State the blood parasite species.
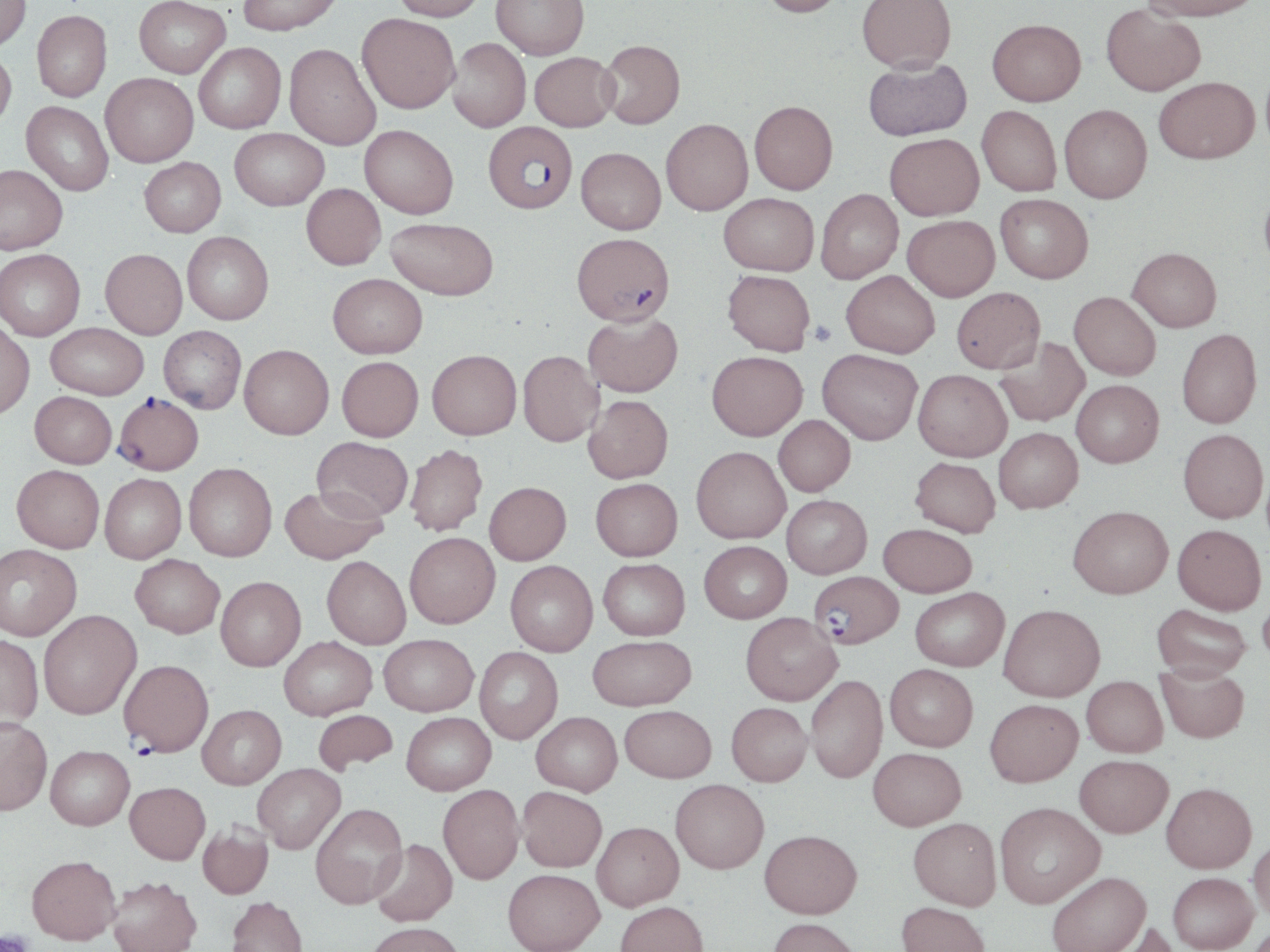

Plasmodium falciparum.

Summary:
  - Coordinate format: approximate bounding boxes as named x1/y1/x2/y2 corners in pixels
  - Platelet locations: (x1=809, y1=320, x2=837, y2=347), (x1=0, y1=931, x2=35, y2=952)
  - Uninfected red blood cell locations: (x1=0, y1=0, x2=31, y2=52), (x1=134, y1=0, x2=230, y2=77), (x1=238, y1=0, x2=343, y2=35), (x1=392, y1=0, x2=487, y2=21), (x1=491, y1=0, x2=589, y2=59), (x1=759, y1=0, x2=847, y2=17), (x1=857, y1=0, x2=956, y2=72), (x1=1142, y1=0, x2=1262, y2=21), (x1=1101, y1=4, x2=1206, y2=96), (x1=32, y1=10, x2=112, y2=101), (x1=357, y1=14, x2=460, y2=113), (x1=987, y1=18, x2=1086, y2=106), (x1=448, y1=38, x2=531, y2=132), (x1=599, y1=40, x2=685, y2=128), (x1=194, y1=42, x2=286, y2=133), (x1=285, y1=44, x2=381, y2=150), (x1=0, y1=49, x2=16, y2=130), (x1=529, y1=51, x2=619, y2=131), (x1=863, y1=57, x2=972, y2=141), (x1=101, y1=73, x2=198, y2=167), (x1=1154, y1=77, x2=1259, y2=163), (x1=750, y1=100, x2=838, y2=194), (x1=21, y1=101, x2=114, y2=196), (x1=1059, y1=104, x2=1152, y2=203), (x1=977, y1=105, x2=1062, y2=196), (x1=661, y1=118, x2=753, y2=215), (x1=360, y1=124, x2=458, y2=219), (x1=230, y1=128, x2=328, y2=210), (x1=885, y1=133, x2=984, y2=220), (x1=576, y1=147, x2=666, y2=234), (x1=140, y1=157, x2=225, y2=237), (x1=0, y1=164, x2=68, y2=255), (x1=1259, y1=182, x2=1270, y2=281), (x1=301, y1=183, x2=385, y2=269), (x1=816, y1=189, x2=903, y2=283), (x1=719, y1=192, x2=819, y2=275), (x1=995, y1=193, x2=1093, y2=282), (x1=902, y1=215, x2=1000, y2=301), (x1=385, y1=218, x2=498, y2=300), (x1=182, y1=231, x2=274, y2=324), (x1=1128, y1=247, x2=1222, y2=332), (x1=0, y1=249, x2=85, y2=340), (x1=100, y1=249, x2=188, y2=338), (x1=723, y1=270, x2=815, y2=355), (x1=842, y1=270, x2=940, y2=358), (x1=328, y1=273, x2=427, y2=358), (x1=951, y1=287, x2=1045, y2=373), (x1=1069, y1=291, x2=1161, y2=379), (x1=583, y1=312, x2=683, y2=397), (x1=0, y1=321, x2=35, y2=418), (x1=46, y1=322, x2=148, y2=399), (x1=158, y1=326, x2=246, y2=413), (x1=1176, y1=328, x2=1262, y2=428), (x1=994, y1=336, x2=1089, y2=426), (x1=239, y1=344, x2=333, y2=439), (x1=817, y1=348, x2=922, y2=444), (x1=427, y1=349, x2=521, y2=439), (x1=518, y1=350, x2=604, y2=446), (x1=707, y1=350, x2=807, y2=440), (x1=337, y1=356, x2=423, y2=441), (x1=913, y1=369, x2=1012, y2=461), (x1=1072, y1=380, x2=1163, y2=467), (x1=30, y1=391, x2=117, y2=468), (x1=583, y1=395, x2=673, y2=482), (x1=774, y1=415, x2=855, y2=496), (x1=994, y1=427, x2=1082, y2=513), (x1=1178, y1=428, x2=1268, y2=523), (x1=312, y1=437, x2=413, y2=522), (x1=405, y1=444, x2=487, y2=536), (x1=691, y1=446, x2=790, y2=543), (x1=910, y1=457, x2=1000, y2=537), (x1=184, y1=463, x2=277, y2=561), (x1=12, y1=464, x2=104, y2=552), (x1=100, y1=473, x2=186, y2=563), (x1=591, y1=478, x2=682, y2=561), (x1=484, y1=481, x2=571, y2=565), (x1=279, y1=485, x2=386, y2=564), (x1=782, y1=494, x2=872, y2=578), (x1=1068, y1=505, x2=1173, y2=598), (x1=879, y1=523, x2=977, y2=597), (x1=1173, y1=524, x2=1266, y2=614), (x1=405, y1=532, x2=500, y2=628), (x1=699, y1=540, x2=792, y2=623), (x1=0, y1=544, x2=82, y2=640), (x1=130, y1=554, x2=225, y2=638), (x1=322, y1=556, x2=411, y2=648), (x1=598, y1=558, x2=690, y2=640), (x1=505, y1=560, x2=597, y2=656), (x1=216, y1=576, x2=306, y2=671), (x1=910, y1=587, x2=1009, y2=671), (x1=1258, y1=588, x2=1270, y2=673), (x1=999, y1=603, x2=1105, y2=701), (x1=1151, y1=604, x2=1252, y2=680), (x1=38, y1=610, x2=141, y2=719), (x1=741, y1=612, x2=841, y2=705), (x1=0, y1=634, x2=43, y2=729), (x1=379, y1=634, x2=478, y2=716), (x1=588, y1=635, x2=696, y2=710), (x1=278, y1=636, x2=377, y2=720), (x1=474, y1=647, x2=563, y2=744), (x1=1156, y1=663, x2=1249, y2=743), (x1=885, y1=664, x2=978, y2=751), (x1=806, y1=674, x2=887, y2=783), (x1=1082, y1=675, x2=1167, y2=757), (x1=985, y1=698, x2=1083, y2=786), (x1=726, y1=702, x2=812, y2=785), (x1=197, y1=704, x2=286, y2=789), (x1=620, y1=704, x2=716, y2=782), (x1=312, y1=709, x2=398, y2=774), (x1=402, y1=711, x2=496, y2=794), (x1=531, y1=711, x2=622, y2=795), (x1=0, y1=716, x2=52, y2=816), (x1=46, y1=745, x2=134, y2=829), (x1=868, y1=747, x2=966, y2=830), (x1=1075, y1=754, x2=1172, y2=837), (x1=252, y1=763, x2=346, y2=853), (x1=670, y1=779, x2=769, y2=873), (x1=125, y1=781, x2=210, y2=864), (x1=1161, y1=782, x2=1257, y2=873), (x1=438, y1=784, x2=524, y2=883), (x1=517, y1=786, x2=607, y2=872), (x1=995, y1=801, x2=1105, y2=907), (x1=310, y1=803, x2=407, y2=908), (x1=909, y1=817, x2=1002, y2=910), (x1=197, y1=821, x2=273, y2=899), (x1=592, y1=821, x2=683, y2=911), (x1=760, y1=829, x2=862, y2=918), (x1=1248, y1=835, x2=1270, y2=924), (x1=370, y1=838, x2=458, y2=926), (x1=26, y1=855, x2=121, y2=944), (x1=503, y1=868, x2=604, y2=952), (x1=1047, y1=871, x2=1151, y2=952), (x1=1168, y1=872, x2=1258, y2=951), (x1=108, y1=875, x2=201, y2=952), (x1=227, y1=895, x2=309, y2=952), (x1=615, y1=900, x2=708, y2=952), (x1=897, y1=900, x2=990, y2=952), (x1=768, y1=917, x2=863, y2=952), (x1=1097, y1=920, x2=1179, y2=952), (x1=367, y1=922, x2=465, y2=952)
  - Plasmodium falciparum-infected red blood cell locations: (x1=483, y1=121, x2=577, y2=213), (x1=572, y1=232, x2=675, y2=326), (x1=114, y1=393, x2=203, y2=475), (x1=810, y1=570, x2=903, y2=649), (x1=119, y1=658, x2=214, y2=756)
  - Image size: 1270×952 pixels
  - Preparation: thin blood smear
  - Field of view: one of a larger specimen
  - Stain: May-Grünwald-Giemsa
  - Modality: light microscopy
  - Magnification: 1000x